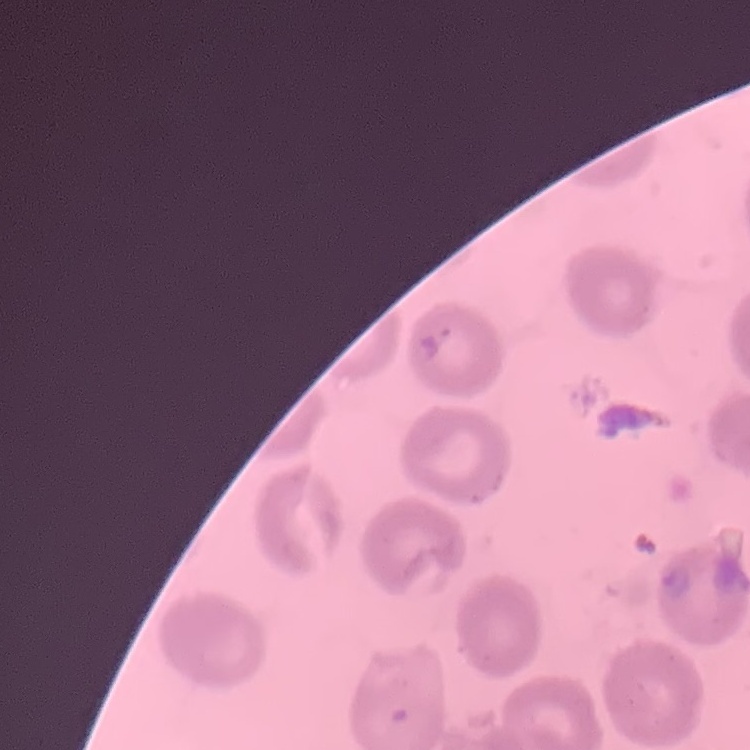
Summary:
  - Red blood cell morphology: no rouleaux formation
  - Image type: one tile cut from a larger photomicrograph
  - Stain: Field's or Giemsa
  - Preparation: thin peripheral smear